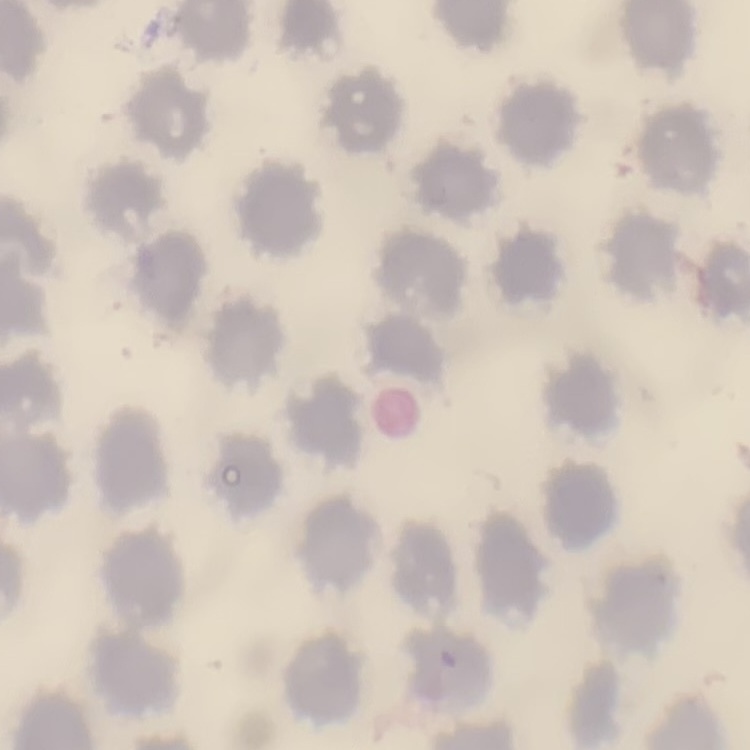

red blood cell morphology = no rouleaux formation
preparation = thin blood smear
stain = Field's or Giemsa
image type = one tile cut from a larger photomicrograph